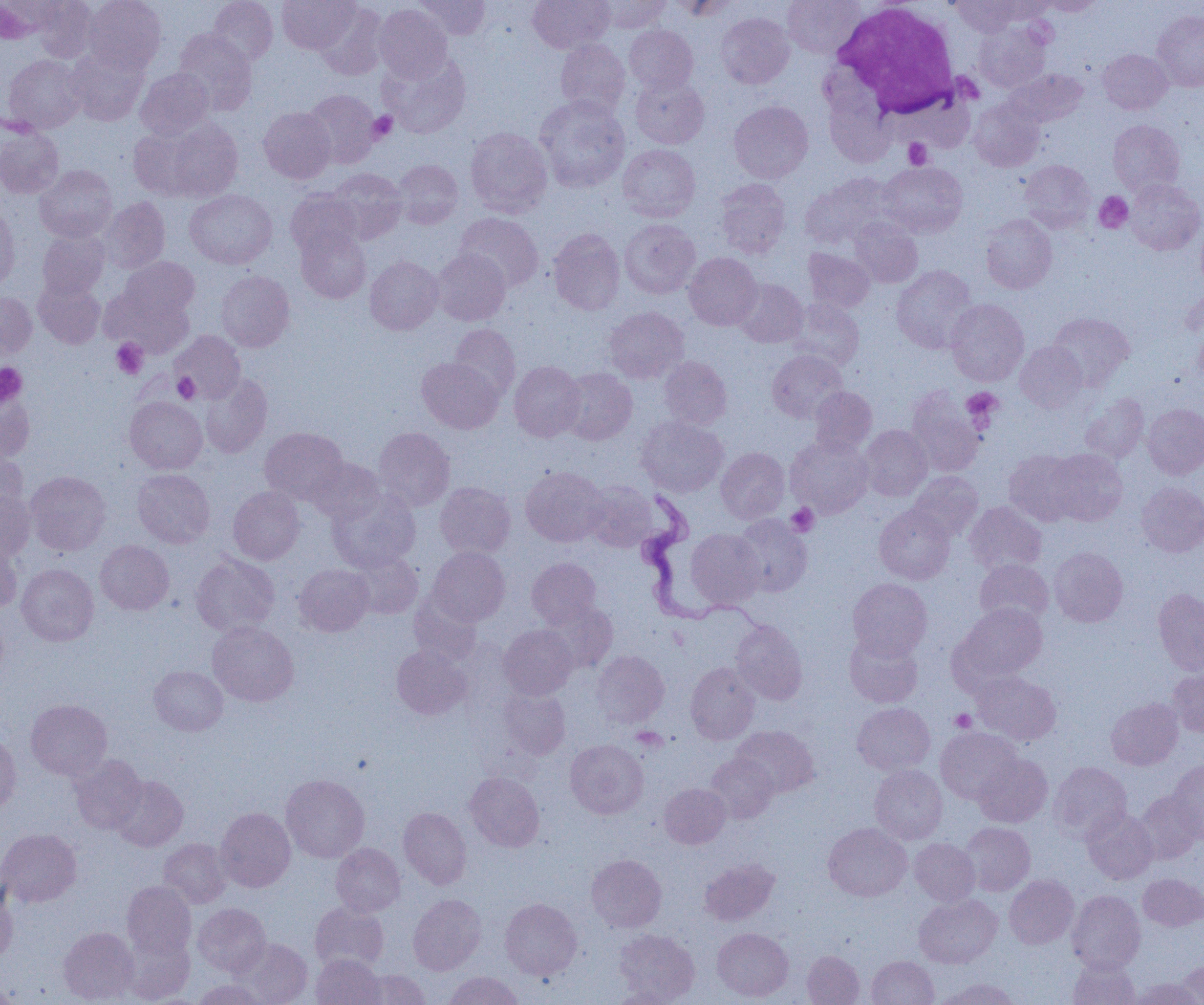

{
  "slide_level_diagnosis": "Trypanosoma brucei",
  "modality": "light microscopy",
  "magnification": "1000x",
  "image_size": "1204×1005 pixels",
  "field_of_view": "single",
  "platelet_locations": "approximate bounding boxes as [x1, y1, x2, y2] in pixels: [368, 111, 397, 143], [904, 138, 932, 169], [1094, 192, 1133, 233], [112, 339, 148, 379], [0, 363, 27, 407], [173, 373, 200, 403], [961, 388, 1002, 426], [786, 503, 819, 536], [951, 709, 976, 733], [631, 727, 668, 753]",
  "preparation": "thin blood film",
  "white_blood_cell_locations": "approximate bounding boxes as [x1, y1, x2, y2] in pixels: [833, 2, 963, 116]",
  "uninfected_red_blood_cell_locations": "approximate bounding boxes as [x1, y1, x2, y2] in pixels: [32, 0, 96, 62], [83, 0, 166, 73], [208, 0, 277, 67], [277, 0, 358, 53], [414, 0, 491, 39], [528, 0, 614, 53], [595, 0, 672, 33], [666, 0, 738, 20], [783, 0, 866, 59], [950, 0, 1025, 36], [1037, 0, 1103, 15], [314, 2, 388, 80], [374, 4, 452, 82], [1152, 11, 1204, 91], [716, 12, 794, 88], [973, 22, 1051, 92], [624, 25, 698, 93], [173, 29, 256, 114], [555, 39, 630, 118], [66, 46, 149, 125], [1098, 49, 1172, 114], [380, 52, 470, 138], [4, 55, 85, 132], [135, 68, 214, 138], [1007, 68, 1088, 127], [630, 74, 709, 149], [303, 89, 380, 168], [534, 96, 630, 192], [969, 99, 1044, 171], [729, 101, 813, 183], [259, 107, 336, 183], [154, 117, 244, 202], [1108, 119, 1185, 195], [0, 126, 64, 199], [128, 126, 201, 199], [466, 127, 552, 217], [618, 144, 700, 221], [392, 159, 463, 228], [1020, 160, 1095, 232], [878, 162, 967, 238], [35, 165, 117, 242], [327, 168, 406, 243], [801, 174, 896, 249], [715, 178, 790, 258], [1126, 179, 1204, 255], [185, 190, 276, 269], [286, 190, 361, 258], [101, 197, 170, 273], [0, 205, 19, 293], [455, 213, 543, 291], [981, 214, 1056, 293], [850, 218, 922, 287], [1196, 218, 1204, 294], [620, 219, 700, 298], [296, 227, 371, 303], [548, 228, 625, 315], [38, 230, 109, 299], [804, 248, 875, 312], [432, 249, 510, 325], [684, 252, 762, 330], [365, 256, 443, 335], [119, 257, 199, 322], [891, 265, 978, 353], [216, 270, 295, 351], [33, 278, 105, 349], [733, 278, 807, 348], [103, 287, 193, 357], [0, 291, 36, 359], [787, 299, 865, 370], [946, 299, 1029, 385], [604, 307, 688, 383], [1048, 313, 1134, 389], [1194, 321, 1204, 386], [449, 323, 520, 399], [172, 331, 245, 402], [1016, 342, 1087, 412], [767, 350, 848, 423], [659, 356, 732, 429], [417, 357, 503, 433], [509, 361, 586, 441], [560, 367, 637, 444], [199, 372, 272, 458], [809, 386, 877, 455], [907, 388, 987, 476], [0, 389, 34, 462], [1080, 393, 1149, 464], [125, 396, 207, 473], [1143, 404, 1204, 478], [636, 416, 728, 497], [859, 425, 932, 500], [260, 427, 348, 504], [373, 427, 454, 511], [786, 435, 873, 518], [0, 445, 27, 515], [716, 447, 789, 523], [1045, 449, 1127, 525], [1004, 450, 1083, 526], [308, 458, 386, 525], [520, 466, 609, 546], [132, 469, 214, 548], [25, 471, 111, 555], [908, 472, 983, 541], [583, 480, 657, 551], [435, 482, 515, 559], [1137, 482, 1204, 557], [228, 486, 304, 564], [0, 490, 35, 559], [329, 490, 420, 572], [965, 501, 1046, 574], [874, 505, 955, 584], [732, 514, 812, 597], [686, 529, 764, 608], [0, 536, 22, 613], [95, 540, 174, 614], [428, 547, 510, 625], [1049, 547, 1128, 626], [348, 549, 423, 619], [191, 554, 280, 636], [527, 557, 601, 627], [974, 559, 1054, 628], [16, 563, 99, 646], [294, 564, 374, 636], [847, 578, 932, 659], [1153, 589, 1204, 674], [409, 590, 483, 666], [540, 601, 617, 673], [955, 602, 1047, 684], [0, 607, 8, 684], [730, 620, 807, 705], [207, 621, 299, 706], [498, 624, 577, 699], [844, 631, 923, 707], [392, 646, 472, 719], [590, 650, 669, 729], [685, 662, 760, 744], [149, 665, 228, 735], [1168, 669, 1204, 736], [973, 671, 1061, 745], [499, 685, 572, 760], [1107, 698, 1183, 770], [26, 699, 112, 780], [852, 703, 935, 774], [732, 725, 819, 798], [936, 727, 1022, 804], [0, 732, 21, 815], [565, 739, 648, 819], [706, 753, 778, 823], [974, 754, 1052, 827], [70, 755, 147, 834], [1168, 760, 1204, 843], [1049, 762, 1131, 841], [870, 765, 947, 843], [465, 772, 544, 851], [280, 774, 370, 863], [110, 775, 188, 851], [660, 783, 731, 848], [1134, 791, 1202, 864], [216, 807, 295, 891], [399, 807, 471, 889], [1082, 808, 1158, 884], [960, 822, 1035, 895], [823, 823, 911, 901], [0, 828, 81, 907], [159, 838, 231, 908], [910, 838, 980, 905], [331, 843, 405, 916], [586, 854, 667, 932], [699, 858, 779, 926], [1138, 873, 1204, 931], [1004, 875, 1079, 948], [122, 881, 196, 960], [0, 885, 17, 962], [1067, 890, 1145, 973], [408, 894, 486, 975], [914, 894, 1002, 968], [500, 898, 582, 980], [310, 902, 389, 973], [193, 903, 271, 977], [59, 927, 139, 1004], [713, 927, 793, 1001], [614, 928, 699, 1002], [122, 932, 194, 1003], [233, 938, 312, 1005], [802, 950, 864, 1005], [311, 954, 386, 1005], [866, 956, 939, 1005], [1068, 958, 1140, 1005], [1175, 961, 1204, 1004], [357, 969, 431, 1004], [444, 971, 524, 1005], [1129, 977, 1200, 1005], [935, 978, 1021, 1005], [193, 980, 268, 1004], [608, 987, 683, 1004]",
  "trypanosoma_brucei_locations": "approximate bounding boxes as [x1, y1, x2, y2] in pixels: [633, 489, 755, 631]"
}